Assess this cell for malaria.
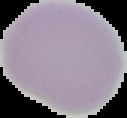

It is uninfected.

Summary:
  - Image size: 127×118 pixels
  - Preparation: thin blood film
  - Image type: segmented cell region with the area outside set to black